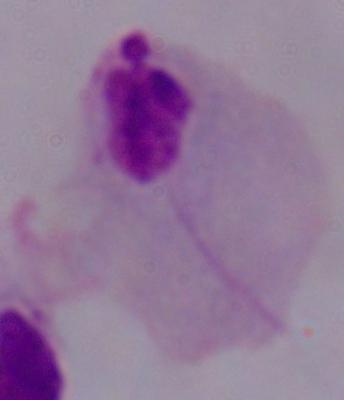
modality = photomicrograph
magnification = 1000x
identification = trichomonad